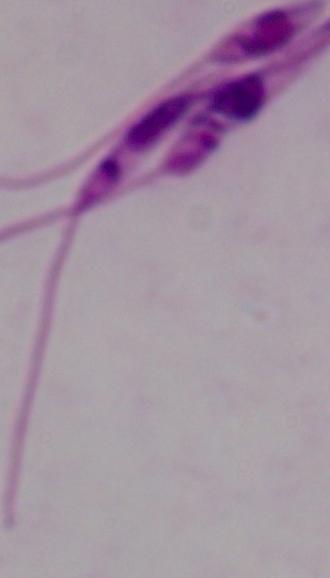

Summary:
  - Identification: Leishmania
  - Magnification: 1000x
  - Modality: photomicrograph